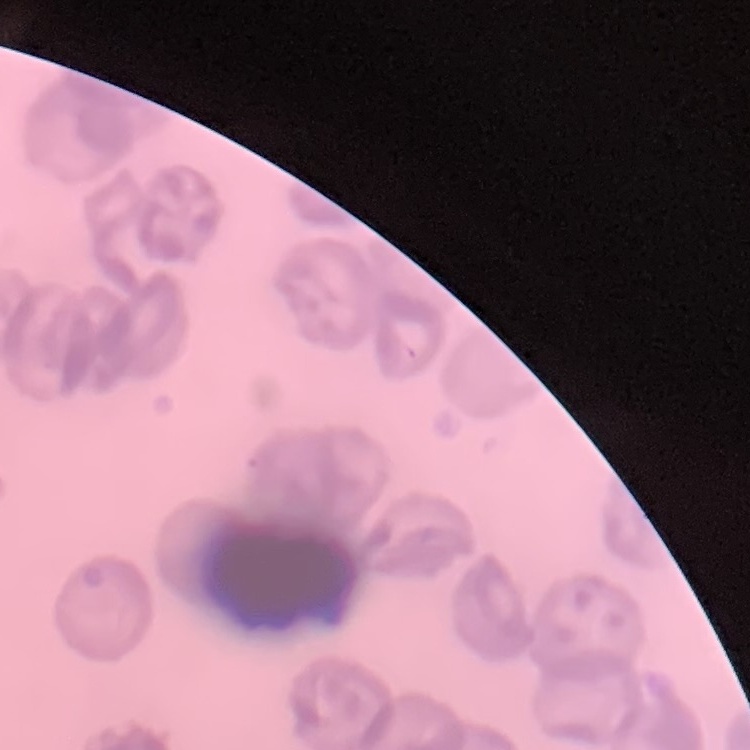

erythrocyte morphology = no rouleaux formation
preparation = thin blood film
stain = Field's or Giemsa
image type = square crop of a larger photomicrograph